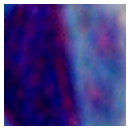 A leukocyte is shown. Photomicrograph. Captured at 1000x magnification.